State the blood parasite species.
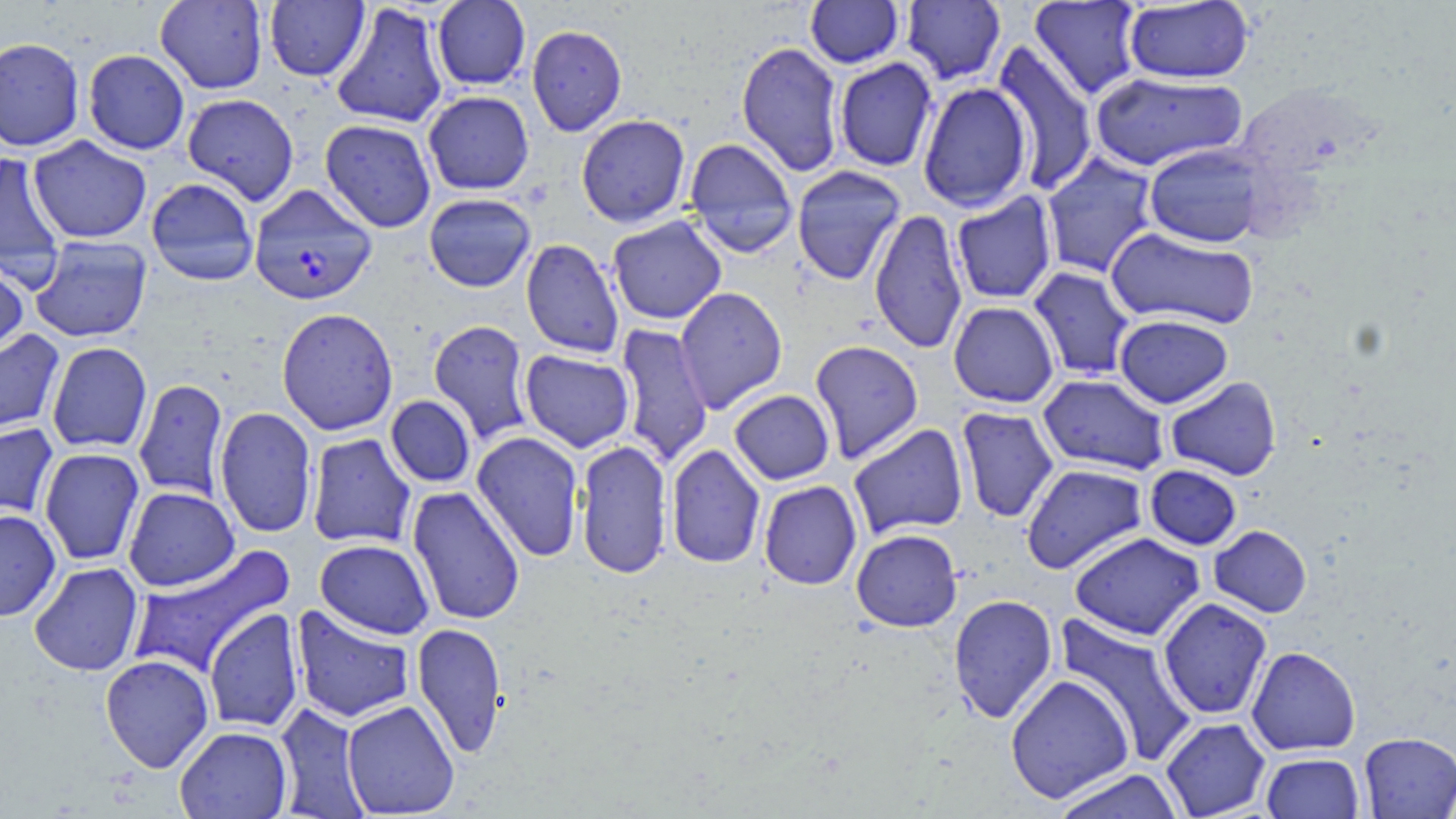
Plasmodium falciparum.

magnification = 1000x
field of view = single
modality = light microscopy
preparation = thin blood film
image size = 1456×819 pixels
uninfected red blood cell locations = approximate bounding boxes as (x1, y1, x2, y2) in pixels: (155, 0, 269, 94), (432, 0, 531, 91), (805, 0, 904, 68), (901, 0, 1006, 85), (264, 1, 370, 82), (1029, 1, 1144, 100), (1124, 1, 1254, 84), (330, 2, 448, 129), (526, 24, 627, 136), (0, 37, 85, 152), (736, 41, 844, 177), (992, 42, 1099, 195), (83, 49, 190, 155), (834, 58, 938, 172), (1090, 71, 1248, 172), (918, 82, 1032, 213), (423, 91, 534, 195), (182, 93, 299, 206), (576, 114, 691, 228), (320, 119, 436, 233), (27, 136, 152, 243), (683, 138, 798, 256), (1144, 144, 1268, 248), (0, 152, 67, 282), (1040, 152, 1159, 279), (791, 165, 907, 285), (146, 177, 259, 286), (951, 192, 1058, 305), (423, 193, 535, 292), (869, 208, 968, 355), (608, 216, 726, 325), (1105, 227, 1259, 330), (29, 235, 152, 343), (521, 238, 624, 358), (0, 259, 29, 359), (1028, 266, 1136, 381), (674, 286, 788, 413), (949, 301, 1059, 407), (277, 307, 398, 436), (1115, 314, 1233, 408), (428, 320, 533, 444), (615, 323, 713, 467), (0, 329, 65, 440), (810, 340, 924, 463), (47, 342, 152, 452), (520, 350, 634, 452), (1039, 374, 1170, 475), (1165, 376, 1282, 481), (133, 378, 229, 502), (729, 390, 834, 484), (386, 395, 476, 488), (214, 406, 317, 539), (956, 407, 1059, 523), (0, 423, 60, 523), (848, 423, 968, 539), (472, 431, 584, 562), (306, 433, 416, 549), (575, 440, 672, 579), (666, 443, 765, 570), (39, 447, 145, 566), (1021, 464, 1148, 574), (1145, 465, 1241, 550), (759, 481, 862, 590), (123, 486, 239, 591), (407, 486, 526, 626), (0, 509, 61, 621), (1209, 525, 1312, 617), (851, 529, 962, 632), (1070, 532, 1205, 641), (315, 539, 434, 639), (126, 544, 296, 680), (29, 562, 144, 676), (948, 593, 1058, 725), (1158, 597, 1272, 720), (291, 605, 416, 724), (204, 607, 304, 733), (1055, 611, 1199, 766), (412, 622, 508, 758), (1246, 646, 1360, 756), (100, 654, 214, 772), (1005, 674, 1134, 802), (341, 700, 459, 817), (274, 702, 370, 818), (1161, 718, 1271, 818), (174, 726, 292, 818), (1358, 732, 1456, 818), (1261, 752, 1364, 818), (1050, 768, 1186, 819)
stain = May-Grünwald-Giemsa
Plasmodium falciparum-infected red blood cell locations = approximate bounding boxes as (x1, y1, x2, y2) in pixels: (249, 184, 377, 306)